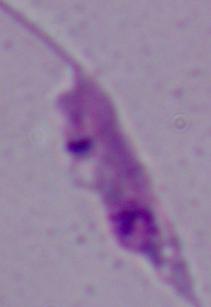

{
  "modality": "photomicrograph",
  "identification": "Leishmania",
  "magnification": "1000x"
}